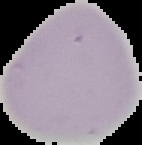
From a thin blood smear. The area outside the segmented cell region is set to black. Result: no malaria parasites detected. Image is 142×145 pixels.